Classify this cell by malaria status.
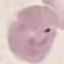
It is parasitized.

Summary:
  - Image type: automatically extracted cell patch, resized to 64 × 64 pixels
  - Preparation: thin smear
  - Stain: Giemsa
  - Capture: smartphone camera at the microscope eyepiece